Assess the morphology of the red blood cells.
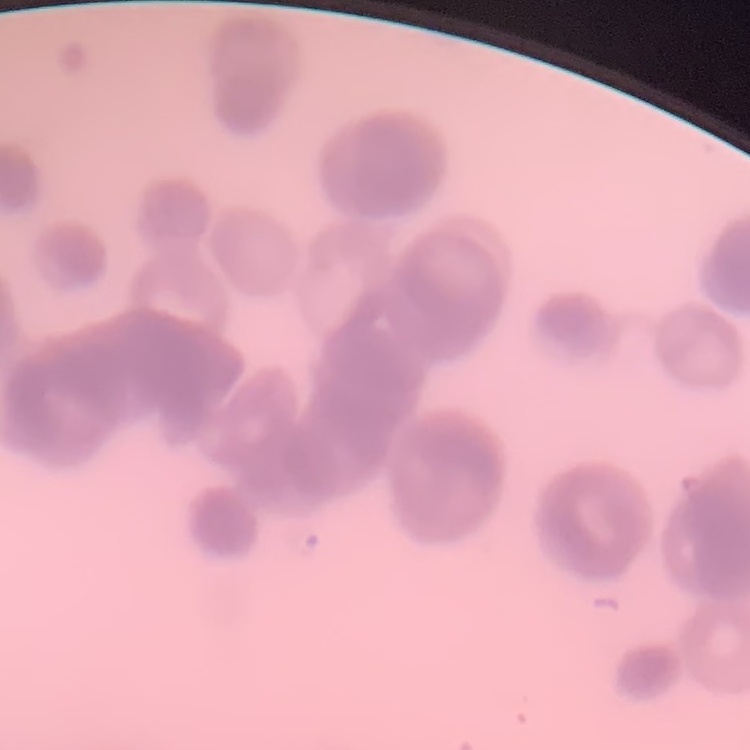

They show rouleaux formation.

Summary:
  - Preparation: thin blood smear
  - Image type: one tile cut from a larger photomicrograph
  - Stain: Field's or Giemsa